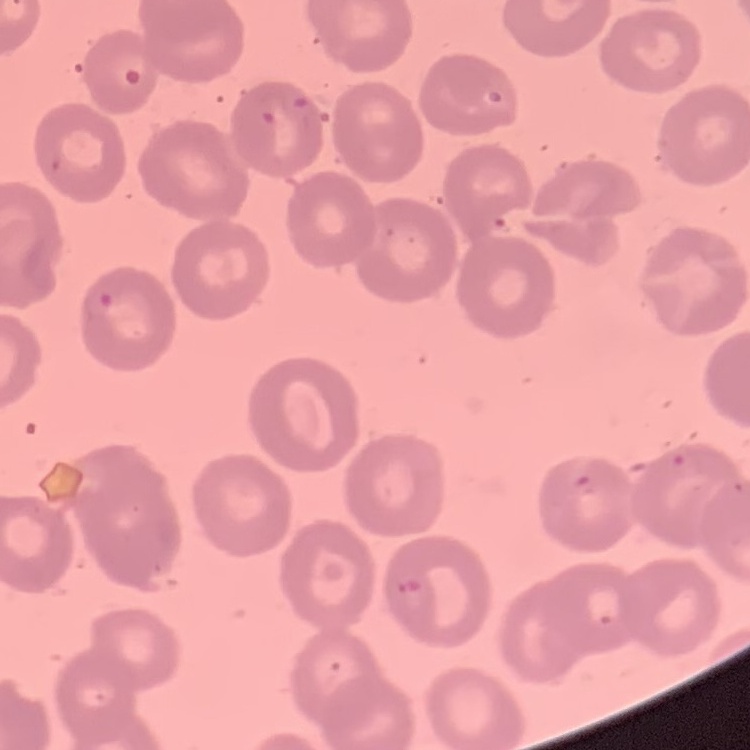
Summary:
  - Red blood cell morphology: no rouleaux formation
  - Preparation: thin peripheral smear
  - Image type: one tile cut from a larger photomicrograph
  - Stain: Field's or Giemsa